Locate and identify every blood parasite.
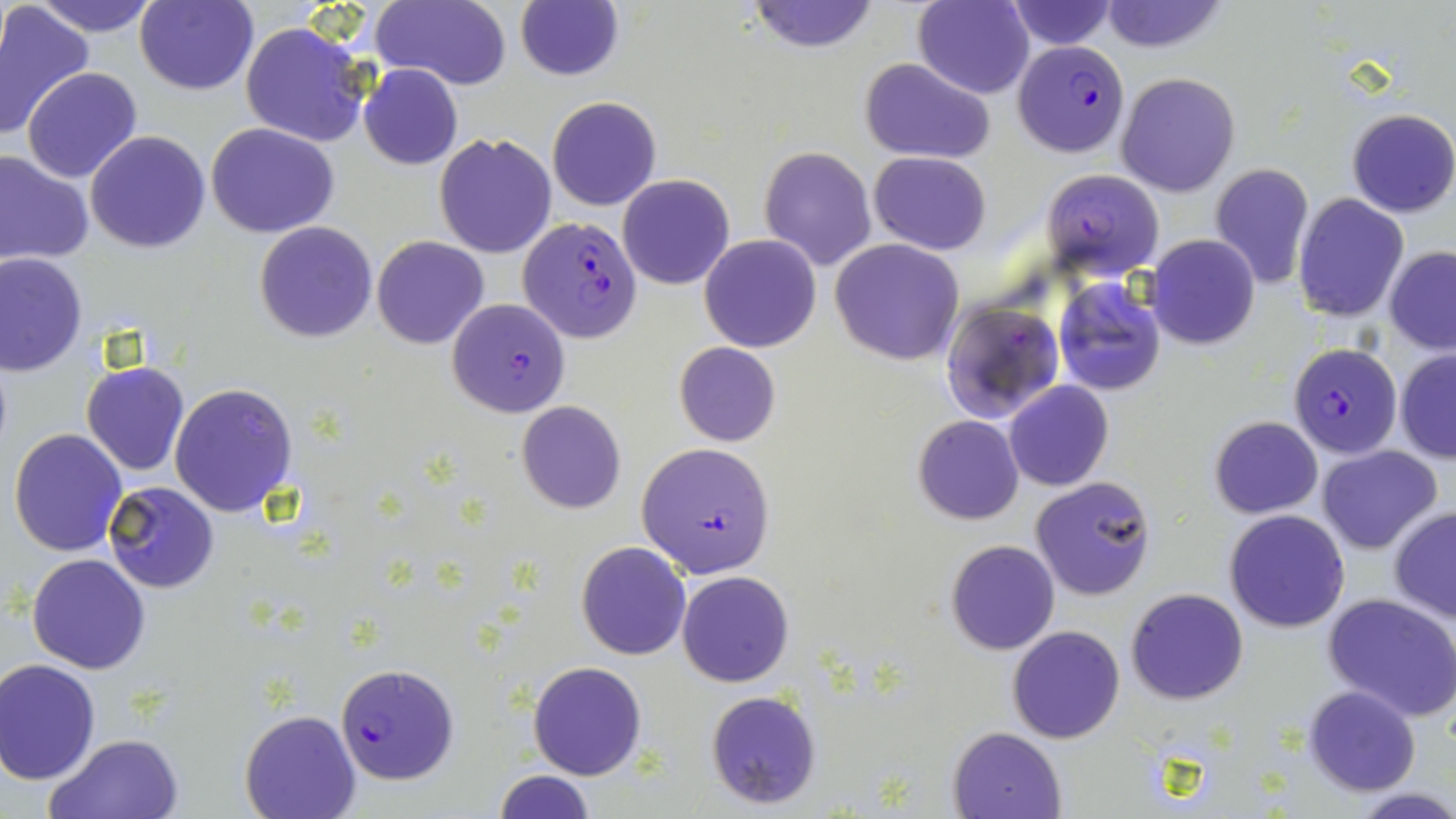

Approximate bounding boxes as (x1,y1)-(x2,y2) corner pairs in pixels.
Plasmodium falciparum-infected red blood cells: (1013,40)-(1131,157), (1041,169)-(1164,279), (516,227)-(639,345), (446,298)-(572,418), (943,300)-(1064,422), (1288,342)-(1402,461), (637,442)-(777,578), (334,662)-(459,785).
No Plasmodium ovale, Plasmodium malariae, Plasmodium vivax, Babesia divergens, or Trypanosoma brucei observed.

Summary:
  - Uninfected red blood cell locations: (30,0)-(159,38), (136,0)-(258,95), (370,0)-(513,91), (747,0)-(880,54), (1097,0)-(1230,54), (912,1)-(1034,99), (1004,1)-(1118,50), (0,3)-(95,139), (515,3)-(624,82), (240,21)-(371,147), (861,58)-(994,164), (359,64)-(463,170), (21,67)-(142,183), (1116,72)-(1240,195), (547,97)-(661,211), (1345,108)-(1456,218), (207,123)-(338,238), (85,130)-(211,253), (435,132)-(557,259), (759,146)-(876,272), (0,149)-(94,265), (868,151)-(991,255), (1208,162)-(1314,290), (618,174)-(734,290), (1293,192)-(1408,321), (254,222)-(378,342), (700,234)-(820,352), (1146,235)-(1260,350), (371,236)-(488,350), (830,238)-(964,366), (1384,246)-(1456,354), (0,252)-(87,376), (1053,278)-(1166,394), (673,342)-(781,448), (1395,349)-(1456,463), (82,361)-(189,475), (1005,381)-(1113,492), (168,382)-(297,518), (516,401)-(626,514), (913,414)-(1024,525), (1210,416)-(1324,519), (8,429)-(127,557), (1316,445)-(1443,554), (1030,476)-(1157,601), (104,481)-(220,594), (1389,506)-(1456,622), (1224,510)-(1350,631), (946,539)-(1061,655), (576,542)-(691,659), (27,554)-(149,675), (677,570)-(794,686), (1126,587)-(1248,705), (1323,593)-(1456,721), (1008,626)-(1125,744), (1,660)-(102,784), (527,660)-(646,780), (1303,686)-(1420,796), (704,689)-(822,809), (240,708)-(360,819), (948,726)-(1065,819), (45,732)-(184,819), (493,771)-(595,818), (1347,787)-(1456,818)
  - Slide-level diagnosis: Plasmodium falciparum
  - Magnification: 1000x
  - Modality: optical microscopy
  - Field of view: one of a larger specimen
  - Stain: May-Grünwald-Giemsa
  - Preparation: thin blood film
  - Image size: 1456×819 pixels